State which parasite is depicted.
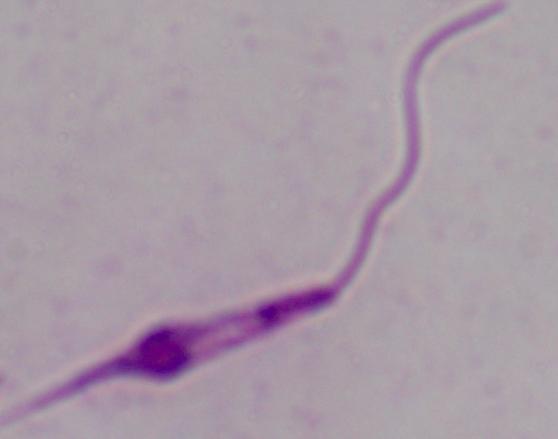
Leishmania.

modality = photomicrograph
magnification = 1000x